Report the malaria status of this cell.
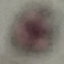
Uninfected.

Thin blood smear. Cell patch, automatically extracted from a larger field of view and resized to 64 × 64 pixels. Acquired by smartphone through the microscope eyepiece. Giemsa stain.